Assess this cell for malaria.
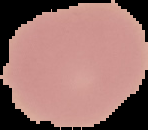

It is uninfected.

{
  "image_size": "148×130 pixels",
  "preparation": "thin blood film",
  "image_type": "segmented cell region with the area outside set to black"
}